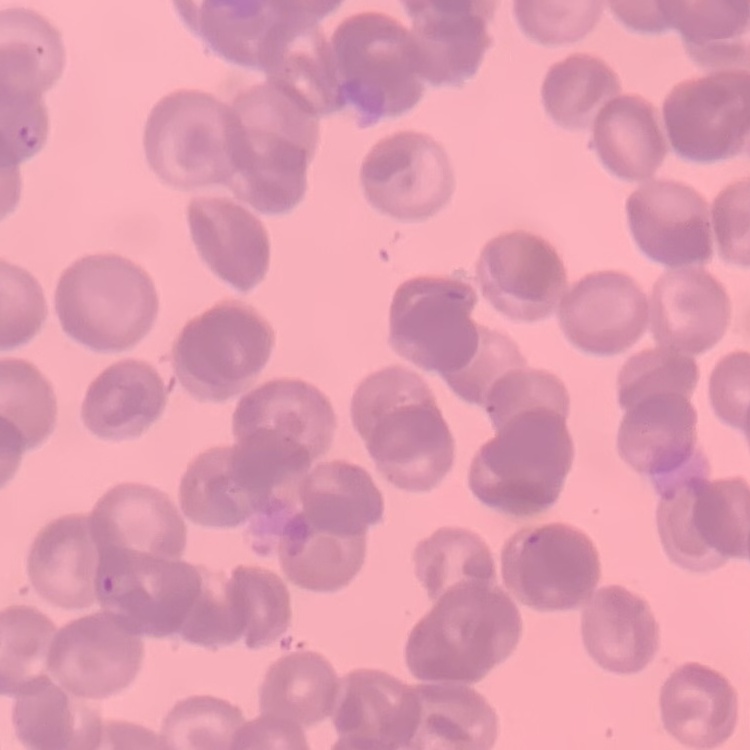 The erythrocytes exhibit rouleaux formation. Field's or Giemsa stain. Square crop of a larger photomicrograph. Thin peripheral smear.